Describe the morphology of the red blood cells.
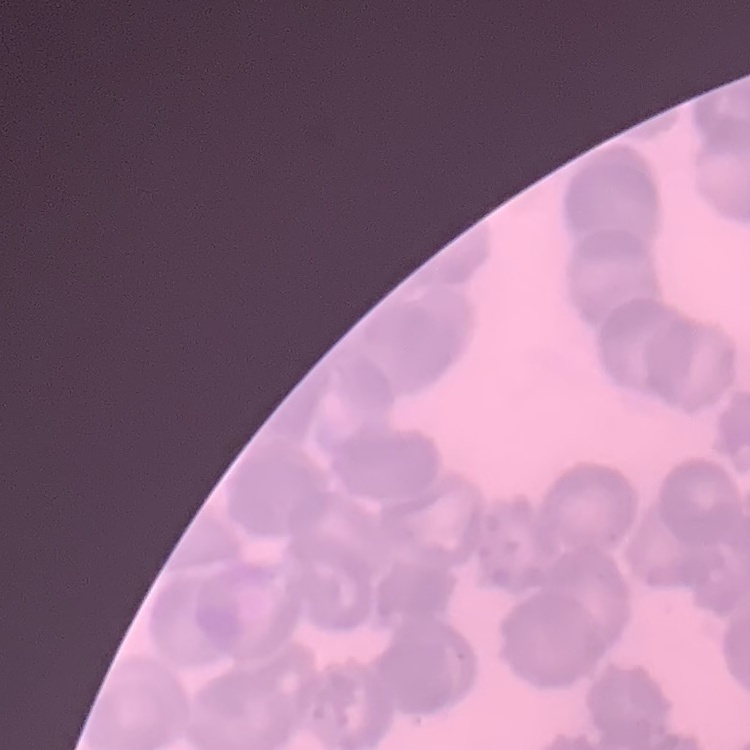

Rouleaux formation.

Stained with either Field's or Giemsa. One tile cut from a larger photomicrograph. Thin blood smear.